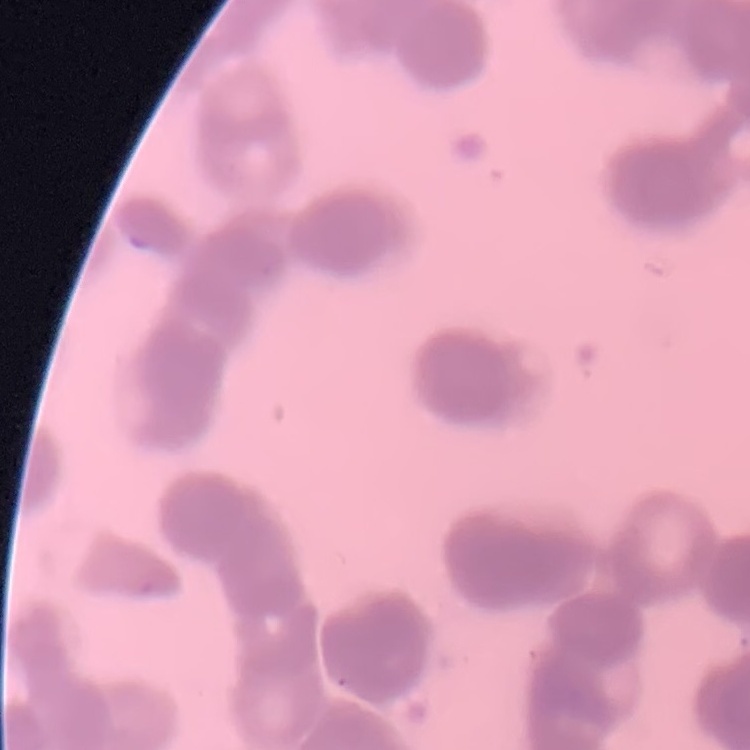

Summary:
  - Red blood cell morphology: rouleaux formation
  - Stain: Field's or Giemsa
  - Preparation: thin blood film
  - Image type: square crop of a larger photomicrograph